Report the malaria status of this cell.
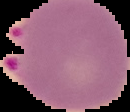
Parasitized.

Cell region segmented out of the field of view; the surrounding area is masked to black. Image is 130×112 pixels. From a thin blood film.